Look for Plasmodium parasites.
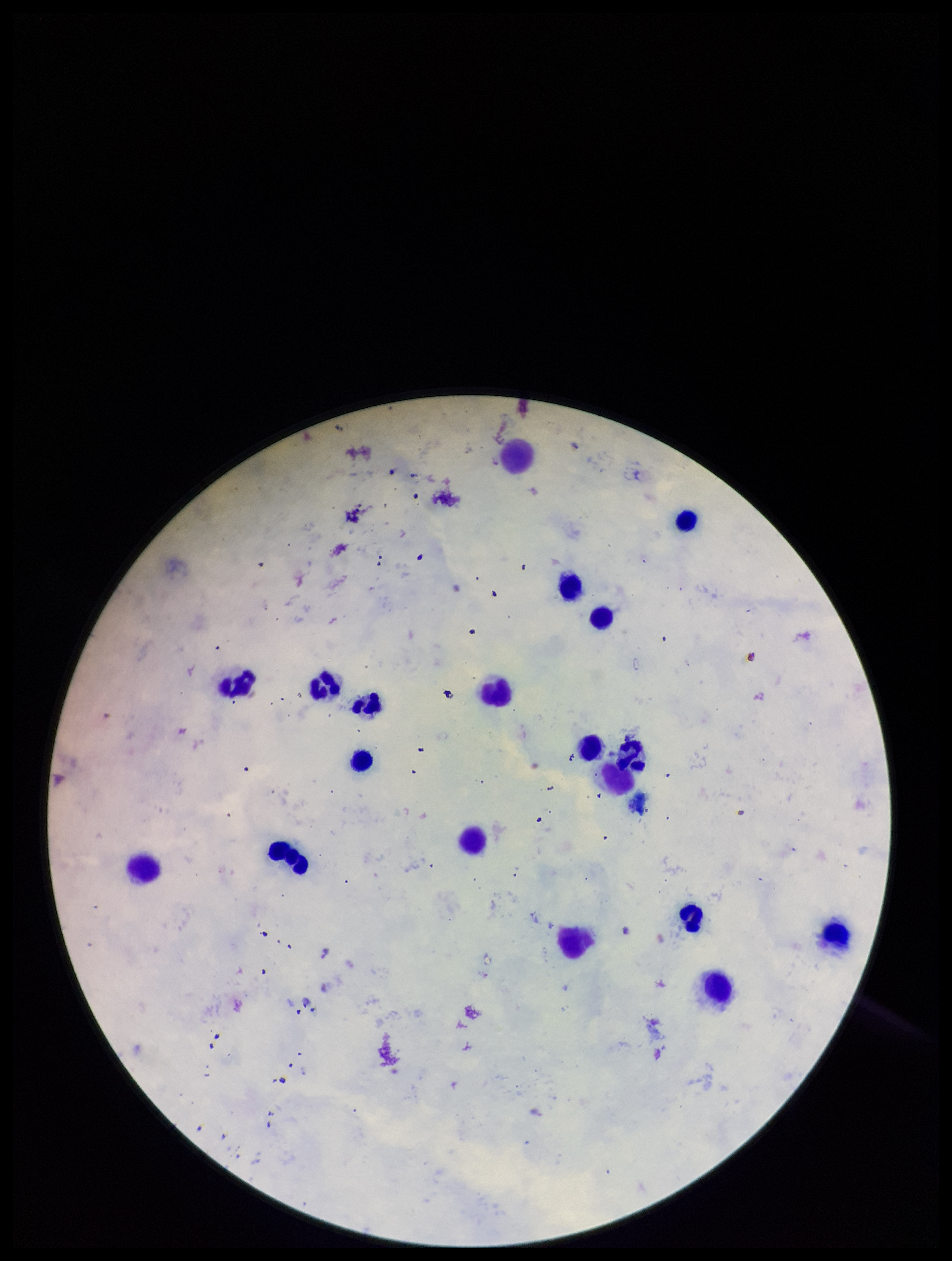
Identified.

Leukocyte count: 19. Species reported for this patient: Plasmodium falciparum. Photographed through the microscope eyepiece with a smartphone camera. Image is 952×1261 pixels. Parasite count: 1. One field from this slide. Giemsa stain. Preparation: thick smear. Patient malaria status: positive.